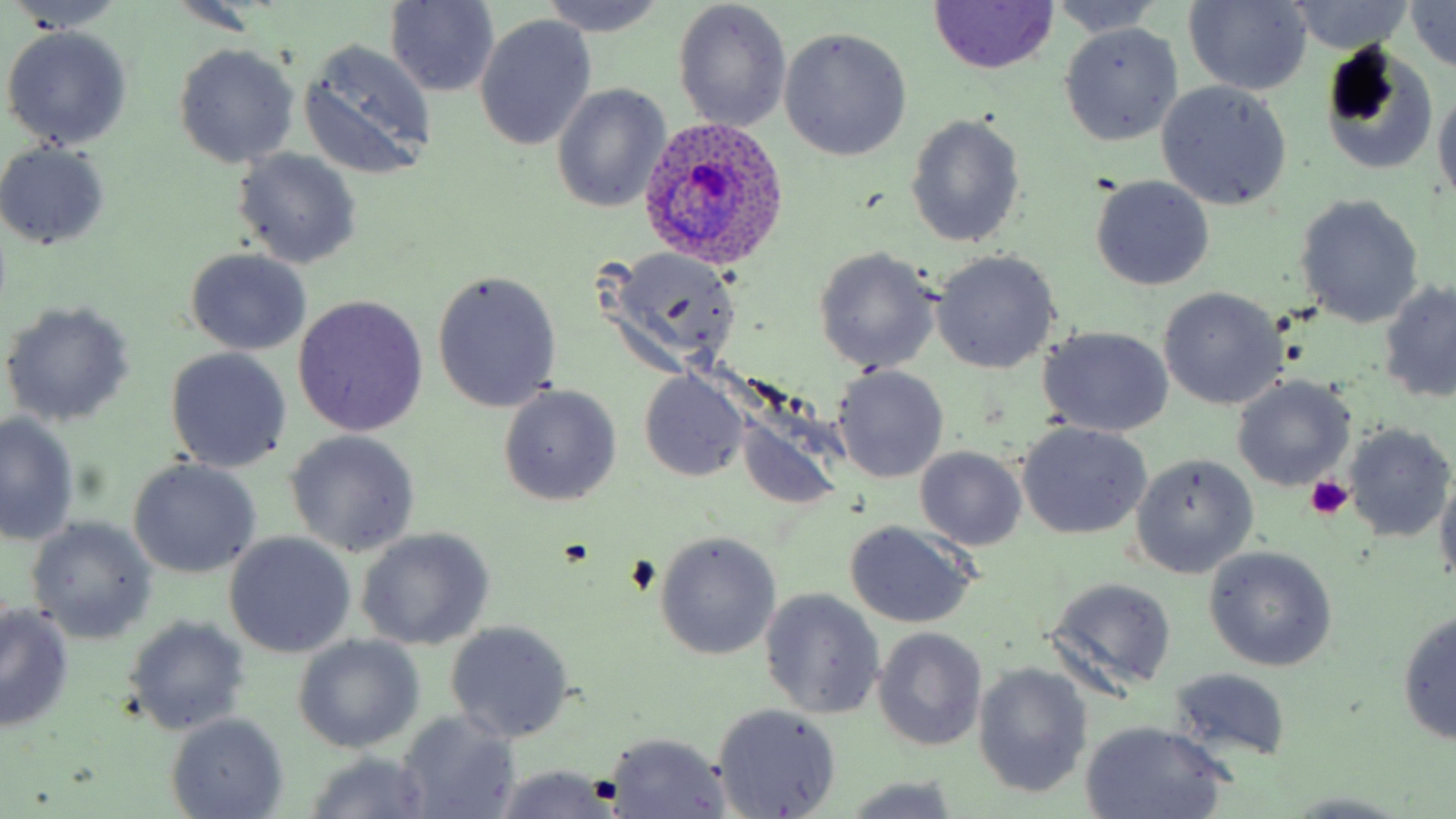
Summary:
  - Coordinate format: approximate bounding boxes as [x1, y1, x2, y2] in pixels
  - Plasmodium ovale-infected red blood cell locations: [641, 116, 796, 273]
  - Uninfected red blood cell locations: [6, 0, 126, 34], [538, 0, 669, 37], [385, 1, 499, 97], [672, 1, 793, 132], [1049, 1, 1164, 38], [1183, 1, 1312, 95], [1286, 1, 1414, 54], [929, 2, 1060, 74], [1406, 2, 1456, 73], [475, 15, 596, 151], [1058, 22, 1184, 146], [2, 25, 134, 150], [779, 27, 912, 161], [298, 39, 437, 179], [1317, 42, 1438, 173], [173, 44, 300, 169], [1155, 80, 1292, 211], [551, 84, 670, 214], [1432, 89, 1456, 209], [906, 114, 1026, 250], [0, 143, 113, 249], [233, 148, 363, 270], [1091, 176, 1216, 292], [1293, 194, 1425, 328], [185, 248, 312, 357], [812, 248, 941, 373], [601, 249, 742, 377], [930, 250, 1062, 374], [432, 268, 562, 413], [1380, 278, 1456, 405], [1158, 287, 1286, 411], [291, 296, 429, 438], [0, 299, 136, 428], [1036, 326, 1174, 438], [164, 347, 292, 472], [830, 364, 950, 484], [640, 372, 748, 481], [1233, 377, 1355, 491], [498, 384, 623, 507], [725, 399, 853, 513], [1, 411, 80, 546], [1343, 421, 1455, 541], [1015, 422, 1152, 541], [285, 430, 420, 557], [916, 446, 1026, 550], [1130, 453, 1258, 579], [127, 458, 261, 579], [1433, 473, 1456, 593], [27, 518, 158, 643], [844, 523, 978, 628], [355, 528, 494, 651], [655, 532, 782, 661], [224, 533, 354, 656], [1204, 547, 1337, 671], [1046, 577, 1177, 694], [761, 589, 884, 718], [0, 604, 76, 733], [1395, 609, 1455, 746], [124, 616, 250, 734], [445, 621, 574, 744], [874, 627, 987, 751], [292, 635, 423, 754], [973, 663, 1093, 799], [1168, 668, 1292, 762], [712, 703, 841, 817], [394, 710, 522, 819], [165, 713, 289, 818], [1079, 720, 1229, 818], [603, 733, 734, 816], [304, 750, 436, 818], [493, 765, 621, 819], [842, 776, 961, 817]
  - Platelet locations: [1305, 474, 1355, 521]
  - Slide-level diagnosis: Plasmodium ovale
  - Magnification: 1000x
  - Stain: May-Grünwald-Giemsa
  - Modality: light microscopy
  - Image size: 1456×819 pixels
  - Field of view: one of a larger specimen
  - Preparation: thin blood film